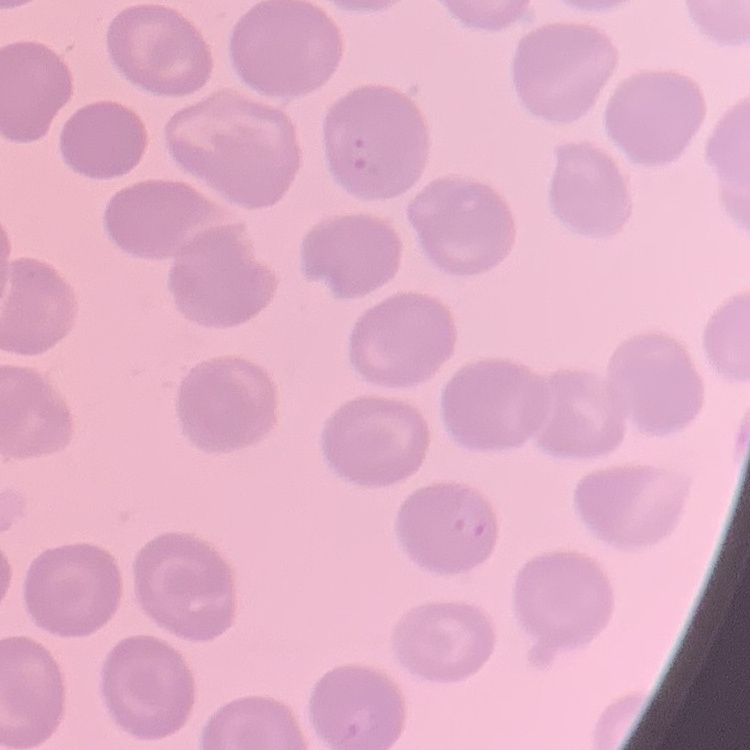

Summary:
  - Erythrocyte morphology: no rouleaux formation
  - Preparation: thin blood film
  - Stain: Field's or Giemsa
  - Image type: one tile cut from a larger photomicrograph